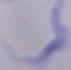

identification = trypanosome
magnification = 1000x
modality = micrograph